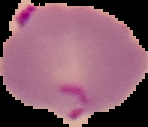

{
  "result": "Plasmodium parasites detected",
  "image_type": "segmented cell region on a black background",
  "image_size": "148×127 pixels",
  "preparation": "thin blood smear"
}